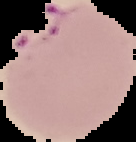

Image is 136×142 pixels. Result: Plasmodium parasites detected. From a thin blood smear. The area outside the segmented cell region is set to black.